Report the malaria status of this cell.
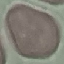
It is uninfected.

Summary:
  - Preparation: thin blood film
  - Image type: cell patch, automatically extracted from a larger field of view and resized to 64 × 64 pixels
  - Capture: smartphone camera at the microscope eyepiece
  - Stain: Giemsa